Identify the blood parasite species.
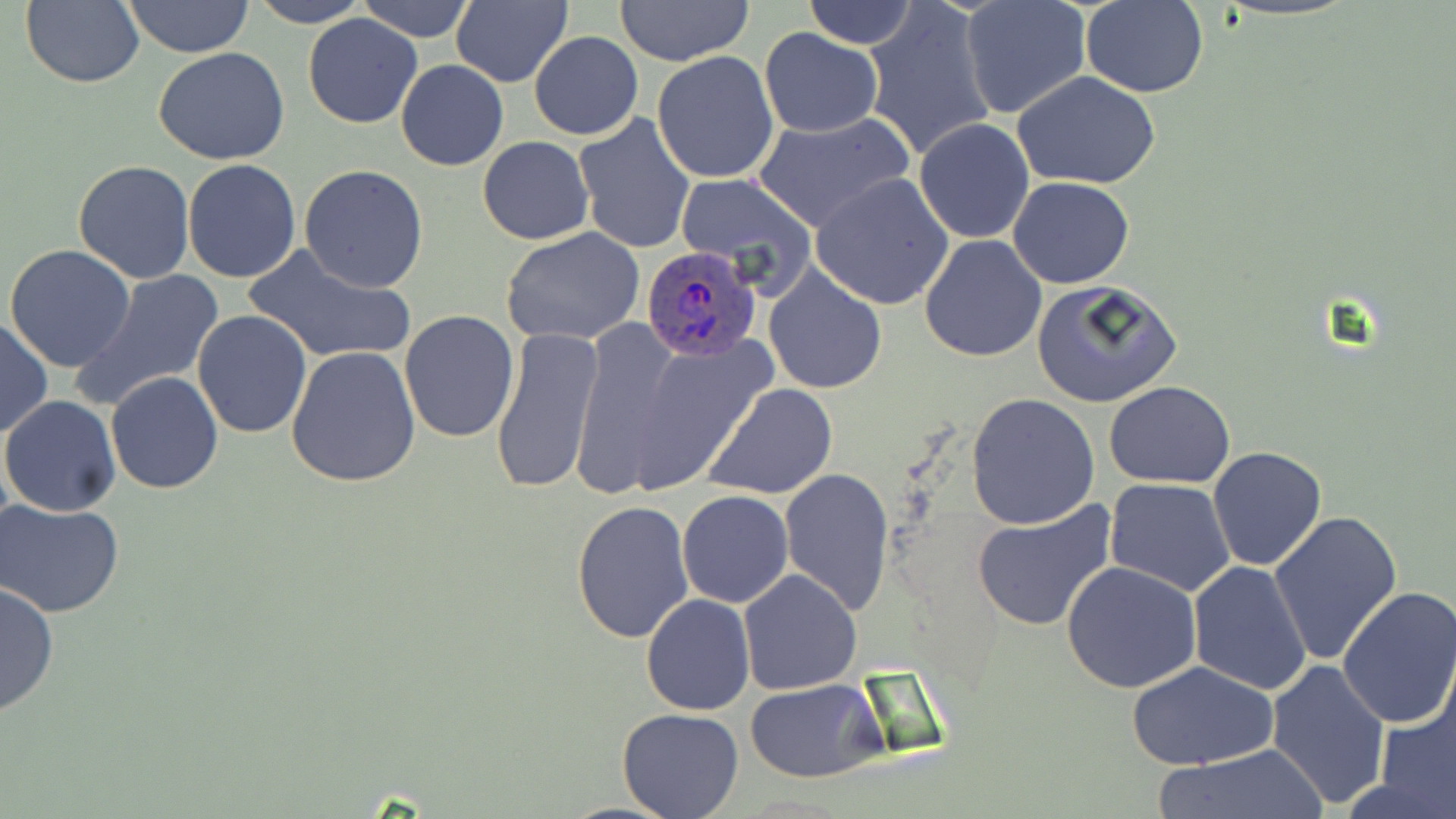

Plasmodium ovale.

Summary:
  - Coordinate format: approximate bounding boxes as (x1,y1)-(x2,y2) corner pairs in pixels
  - Plasmodium ovale-infected red blood cell locations: (638,245)-(763,361)
  - Uninfected red blood cell locations: (21,0)-(146,89), (122,0)-(255,58), (247,0)-(368,27), (357,0)-(475,43), (452,0)-(574,89), (613,0)-(756,67), (801,0)-(917,50), (959,1)-(1091,120), (1081,2)-(1209,97), (863,3)-(999,163), (302,12)-(424,128), (758,28)-(884,137), (530,31)-(643,141), (154,47)-(292,165), (652,51)-(779,184), (395,59)-(508,171), (1012,72)-(1161,189), (751,111)-(916,234), (572,113)-(695,254), (913,118)-(1036,244), (477,136)-(593,244), (182,158)-(302,283), (73,159)-(195,284), (299,165)-(429,291), (674,173)-(816,293), (811,173)-(955,309), (1008,176)-(1135,289), (502,227)-(647,349), (918,234)-(1047,363), (244,242)-(415,365), (4,245)-(137,372), (763,266)-(887,395), (76,269)-(228,411), (1030,279)-(1182,408), (191,310)-(313,438), (399,310)-(519,443), (0,316)-(52,439), (567,316)-(688,500), (488,323)-(604,496), (622,331)-(778,492), (285,345)-(422,488), (105,372)-(225,493), (1105,381)-(1235,488), (702,382)-(839,500), (967,392)-(1100,529), (1,395)-(122,517), (1206,447)-(1327,572), (778,466)-(895,616), (1105,479)-(1236,599), (677,490)-(793,608), (571,499)-(695,643), (2,500)-(125,618), (971,501)-(1117,633), (1268,509)-(1403,666), (1061,560)-(1201,694), (1186,561)-(1312,695), (736,568)-(863,696), (0,581)-(58,718), (1335,587)-(1456,730), (640,595)-(755,716), (1126,659)-(1280,769), (1266,659)-(1391,808), (746,680)-(884,782), (1373,688)-(1455,819), (616,708)-(745,819), (1152,747)-(1328,819)
  - Modality: optical microscopy
  - Preparation: thin blood smear
  - Magnification: 1000x
  - Stain: May-Grünwald-Giemsa
  - Field of view: one of a larger specimen
  - Image size: 1456×819 pixels